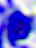

Photomicrograph. Captured at 400x magnification. A leukocyte is shown.